Evaluate for Plasmodium parasites.
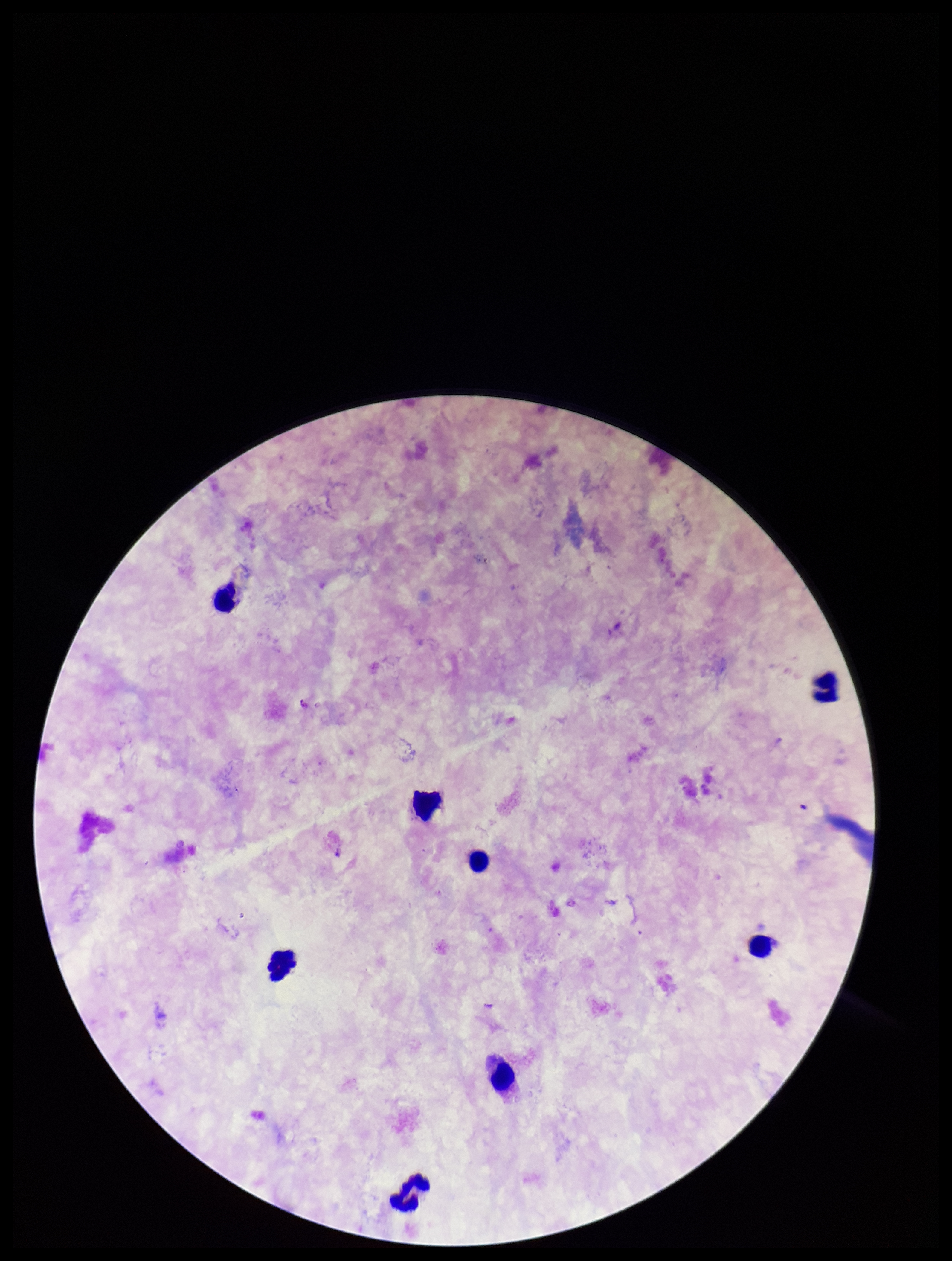
None detected.

Summary:
  - Stain: Giemsa
  - Patient malaria status: negative
  - Parasite count: 0
  - Leukocyte count: 8
  - Capture: smartphone photograph through the microscope eyepiece
  - Field of view: single
  - Image size: 952×1261 pixels
  - Preparation: thick